Report the malaria status of this cell.
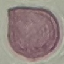

It is uninfected.

Giemsa-stained preparation. Thin blood film. Cell patch, automatically extracted from a larger field of view and resized to 64 × 64 pixels. Photographed with a smartphone camera at the microscope eyepiece.